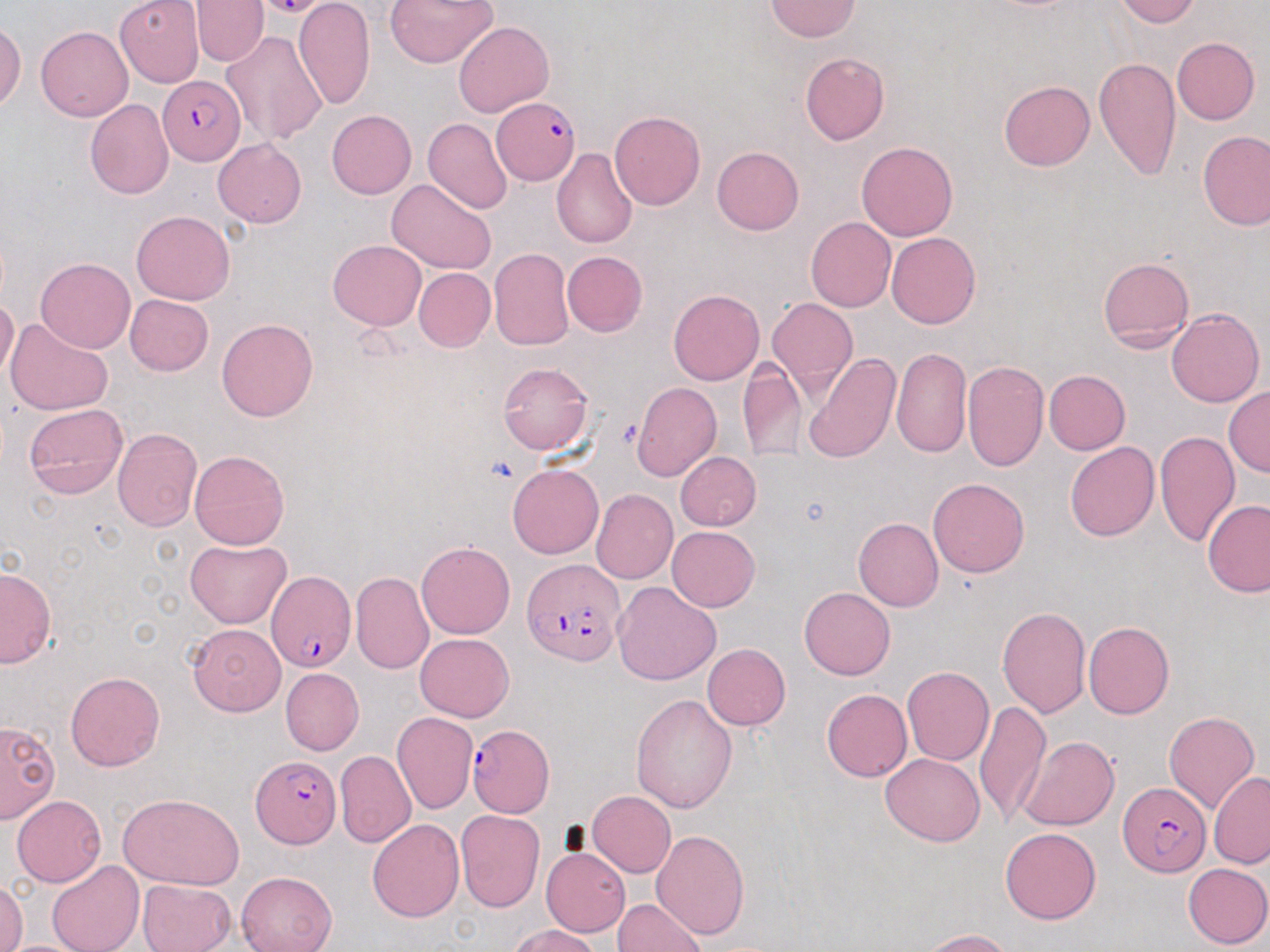
slide-level diagnosis = Plasmodium falciparum
image size = 1270×952 pixels
stain = May-Grünwald-Giemsa
modality = light microscopy
Plasmodium falciparum-infected red blood cell locations = approximate bounding boxes as (x1,y1)-(x2,y2) corner pairs in pixels: (158,76)-(244,164), (493,98)-(579,183), (522,558)-(625,665), (266,567)-(358,673), (467,724)-(554,817), (251,754)-(340,848), (1118,783)-(1210,878)
platelet locations = approximate bounding boxes as (x1,y1)-(x2,y2) corner pairs in pixels: (614,418)-(645,449)
magnification = 1000x
field of view = one of a larger specimen
preparation = thin blood smear
uninfected red blood cell locations = approximate bounding boxes as (x1,y1)-(x2,y2) corner pairs in pixels: (294,0)-(376,111), (383,0)-(497,68), (1114,0)-(1201,27), (115,1)-(204,86), (190,1)-(269,66), (766,1)-(859,41), (454,20)-(554,117), (0,21)-(24,112), (36,26)-(133,122), (222,30)-(328,146), (1172,37)-(1259,124), (800,52)-(888,146), (1092,56)-(1182,182), (1000,80)-(1095,170), (85,99)-(174,199), (327,110)-(416,199), (609,111)-(705,211), (424,118)-(513,214), (1197,130)-(1269,231), (213,138)-(306,227), (856,142)-(958,240), (712,146)-(804,234), (552,147)-(638,249), (386,179)-(496,274), (133,210)-(235,305), (806,217)-(896,312), (886,232)-(980,329), (328,239)-(426,329), (489,247)-(574,350), (562,251)-(648,337), (36,257)-(135,353), (1098,257)-(1194,350), (414,268)-(495,351), (669,288)-(764,385), (125,295)-(213,376), (0,297)-(19,382), (768,299)-(858,396), (1166,307)-(1264,407), (5,319)-(112,415), (217,319)-(317,422), (891,346)-(972,457), (803,353)-(899,464), (961,360)-(1049,473), (738,361)-(806,462), (498,362)-(592,456), (1043,370)-(1129,455), (631,382)-(722,481), (1224,386)-(1270,478), (23,402)-(127,500), (112,429)-(202,531), (1154,429)-(1240,547), (1065,442)-(1159,541), (189,451)-(290,551), (676,452)-(762,530), (507,463)-(604,559), (928,477)-(1030,577), (591,489)-(677,583), (1202,499)-(1270,597), (854,518)-(943,612), (667,527)-(760,611), (186,539)-(292,627), (416,540)-(515,639), (0,567)-(56,668), (352,572)-(434,675), (612,582)-(720,685), (799,587)-(894,680), (997,607)-(1090,716), (1084,620)-(1174,719), (187,623)-(286,716), (415,633)-(515,722), (704,643)-(790,730), (280,667)-(364,754), (902,667)-(994,766), (66,672)-(164,771), (821,689)-(912,781), (631,692)-(738,814), (974,700)-(1049,827), (1164,711)-(1259,814), (392,712)-(477,814), (0,721)-(60,824), (1019,735)-(1119,830), (335,750)-(416,848), (881,752)-(984,846), (1209,771)-(1270,868), (587,791)-(675,878), (118,792)-(245,890), (12,794)-(108,887), (456,810)-(544,912), (367,818)-(465,922), (1001,827)-(1101,925), (652,829)-(750,940), (542,847)-(630,937), (47,860)-(144,952), (1183,862)-(1269,948), (235,871)-(337,952), (136,879)-(236,952), (0,880)-(28,952), (613,898)-(708,951), (510,924)-(599,952), (922,928)-(1016,952)